Find each parasitized RBC.
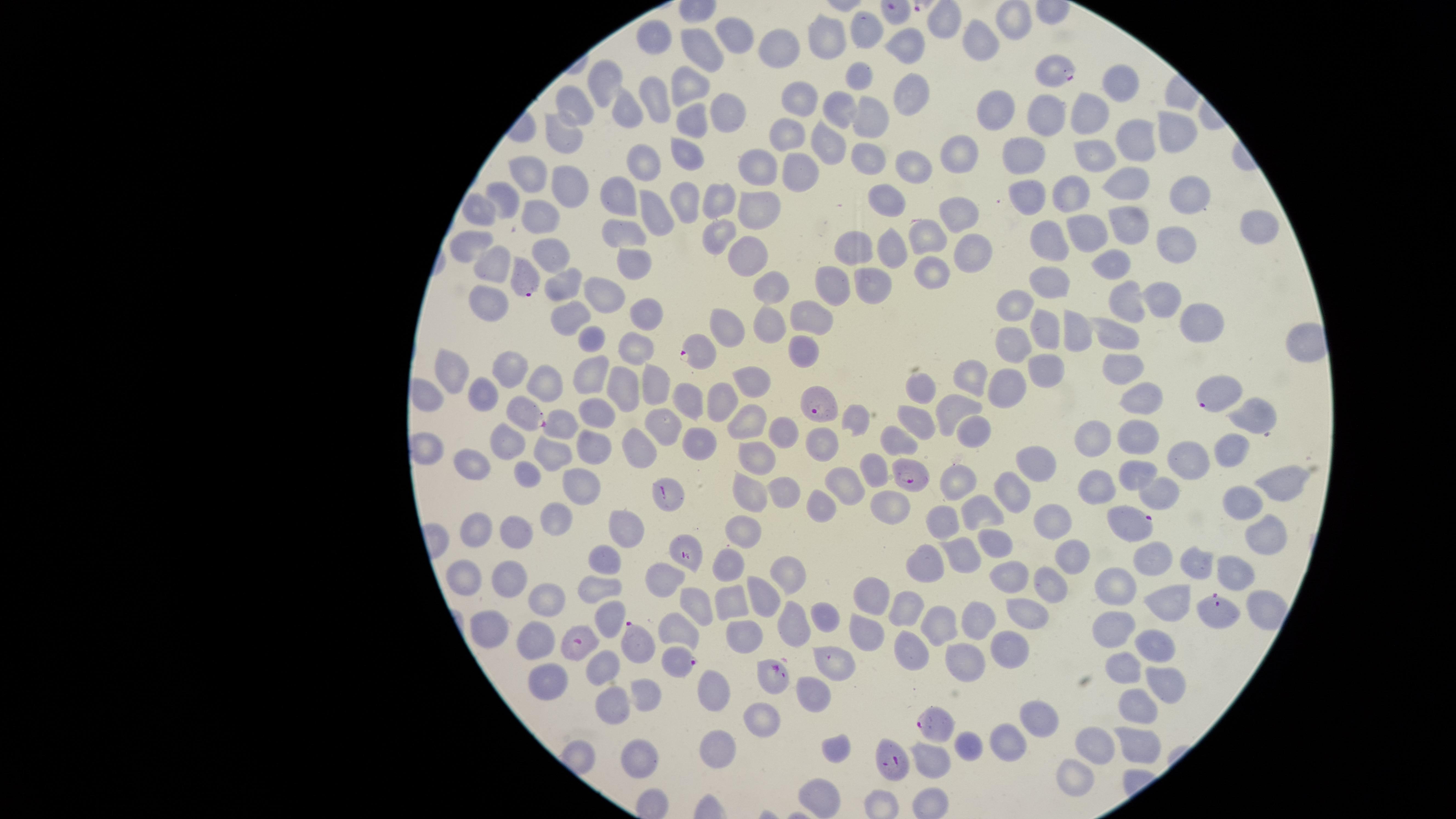
Approximate marker points, in pixels from the top-left corner.
Parasitized RBCs: (x=1056, y=70), (x=527, y=276), (x=699, y=349), (x=1215, y=394), (x=819, y=410), (x=1254, y=411), (x=529, y=415), (x=908, y=475), (x=668, y=491), (x=1130, y=522), (x=686, y=554), (x=1223, y=612), (x=578, y=640), (x=635, y=640), (x=679, y=661), (x=769, y=674), (x=940, y=720), (x=893, y=762).

Approximate marker points, in pixels from the top-left corner. Uninfected RBCs: (x=947, y=21), (x=1013, y=23), (x=867, y=30), (x=733, y=31), (x=661, y=34), (x=828, y=35), (x=978, y=41), (x=912, y=45), (x=783, y=46), (x=705, y=53), (x=856, y=78), (x=1122, y=81), (x=608, y=83), (x=686, y=86), (x=908, y=91), (x=656, y=94), (x=804, y=98), (x=578, y=102), (x=842, y=109), (x=624, y=112), (x=723, y=113), (x=1050, y=113), (x=1092, y=115), (x=993, y=116), (x=865, y=119), (x=687, y=123), (x=789, y=131), (x=1180, y=131), (x=561, y=133), (x=1134, y=138), (x=828, y=145), (x=958, y=151), (x=1025, y=154), (x=1095, y=154), (x=686, y=157), (x=641, y=161), (x=865, y=161), (x=915, y=161), (x=760, y=162), (x=527, y=176), (x=800, y=177), (x=1129, y=185), (x=572, y=186), (x=1075, y=189), (x=509, y=193), (x=886, y=193), (x=1030, y=197), (x=1185, y=197), (x=616, y=198), (x=683, y=198), (x=719, y=198), (x=760, y=205), (x=482, y=209), (x=649, y=212), (x=542, y=215), (x=959, y=215), (x=1131, y=227), (x=626, y=230), (x=719, y=230), (x=1086, y=230), (x=1254, y=230), (x=1052, y=235), (x=923, y=236), (x=859, y=241), (x=472, y=243), (x=892, y=245), (x=1175, y=245), (x=969, y=250), (x=552, y=254), (x=748, y=254), (x=1112, y=262), (x=631, y=263), (x=501, y=265), (x=931, y=278), (x=1050, y=282), (x=566, y=283), (x=874, y=283), (x=832, y=284), (x=772, y=286), (x=602, y=291), (x=1163, y=293), (x=1123, y=298), (x=487, y=300), (x=1020, y=300), (x=645, y=314), (x=571, y=315), (x=809, y=315), (x=1190, y=318), (x=728, y=324), (x=773, y=328), (x=1114, y=330), (x=1045, y=331), (x=1073, y=333), (x=590, y=340), (x=1012, y=345), (x=631, y=347), (x=806, y=348), (x=1047, y=362), (x=452, y=365), (x=1119, y=365), (x=511, y=368), (x=587, y=371), (x=973, y=372), (x=548, y=379), (x=752, y=379), (x=626, y=382), (x=1009, y=384), (x=652, y=385), (x=917, y=387), (x=428, y=395), (x=484, y=398), (x=685, y=398), (x=726, y=399), (x=1144, y=400), (x=957, y=407), (x=589, y=409), (x=748, y=423), (x=920, y=424), (x=664, y=425), (x=561, y=426), (x=972, y=426), (x=783, y=435), (x=1138, y=435), (x=1097, y=437), (x=708, y=441), (x=510, y=442), (x=820, y=442), (x=589, y=446), (x=641, y=446), (x=1230, y=449), (x=427, y=450), (x=558, y=453), (x=760, y=455), (x=1040, y=460), (x=1183, y=461), (x=464, y=464), (x=874, y=465), (x=1133, y=469), (x=528, y=476), (x=848, y=480), (x=960, y=480), (x=583, y=483), (x=1097, y=486), (x=788, y=487), (x=1009, y=487), (x=1285, y=487), (x=1158, y=495), (x=751, y=496), (x=1247, y=501), (x=817, y=504), (x=984, y=509), (x=888, y=511), (x=550, y=518), (x=481, y=520), (x=1049, y=522), (x=946, y=523), (x=627, y=527), (x=742, y=527), (x=515, y=531), (x=1268, y=533), (x=994, y=546), (x=960, y=557), (x=1067, y=558), (x=726, y=559), (x=1149, y=560), (x=1193, y=561), (x=606, y=563), (x=923, y=565), (x=1239, y=572), (x=790, y=574), (x=1009, y=575), (x=669, y=577), (x=508, y=580), (x=461, y=582), (x=1114, y=586), (x=597, y=588), (x=1045, y=592), (x=764, y=594), (x=872, y=594), (x=732, y=598), (x=1174, y=598), (x=550, y=600), (x=696, y=604), (x=1263, y=606), (x=907, y=612), (x=1027, y=613), (x=819, y=615), (x=608, y=617), (x=975, y=622), (x=789, y=625), (x=495, y=626), (x=942, y=626), (x=1115, y=626), (x=867, y=628), (x=680, y=631), (x=537, y=638), (x=732, y=638), (x=1008, y=643), (x=1158, y=647), (x=966, y=652), (x=906, y=653), (x=833, y=665), (x=602, y=669), (x=1119, y=669), (x=548, y=679), (x=1165, y=684), (x=714, y=688), (x=642, y=696), (x=813, y=696), (x=614, y=703), (x=1135, y=711), (x=1038, y=716), (x=764, y=720), (x=1006, y=740), (x=714, y=743), (x=1093, y=743), (x=1137, y=743), (x=833, y=749), (x=960, y=750), (x=644, y=759), (x=929, y=761), (x=1077, y=778), (x=819, y=799). One field of view of the specimen. Giemsa stain. Thin blood film. Photographed with a smartphone camera through the microscope eyepiece. The visible region is circular. Species: Plasmodium falciparum. Image is 1456×819 pixels.